Classify this cell by malaria status.
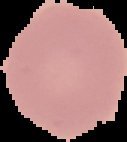
It is uninfected.

From a thin blood film. Image is 127×142 pixels. Segmented cell region on a black background.